Name the parasite shown.
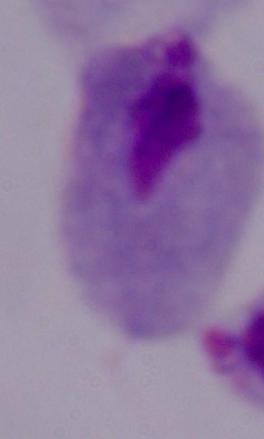

A trichomonad.

Summary:
  - Magnification: 1000x
  - Modality: micrograph